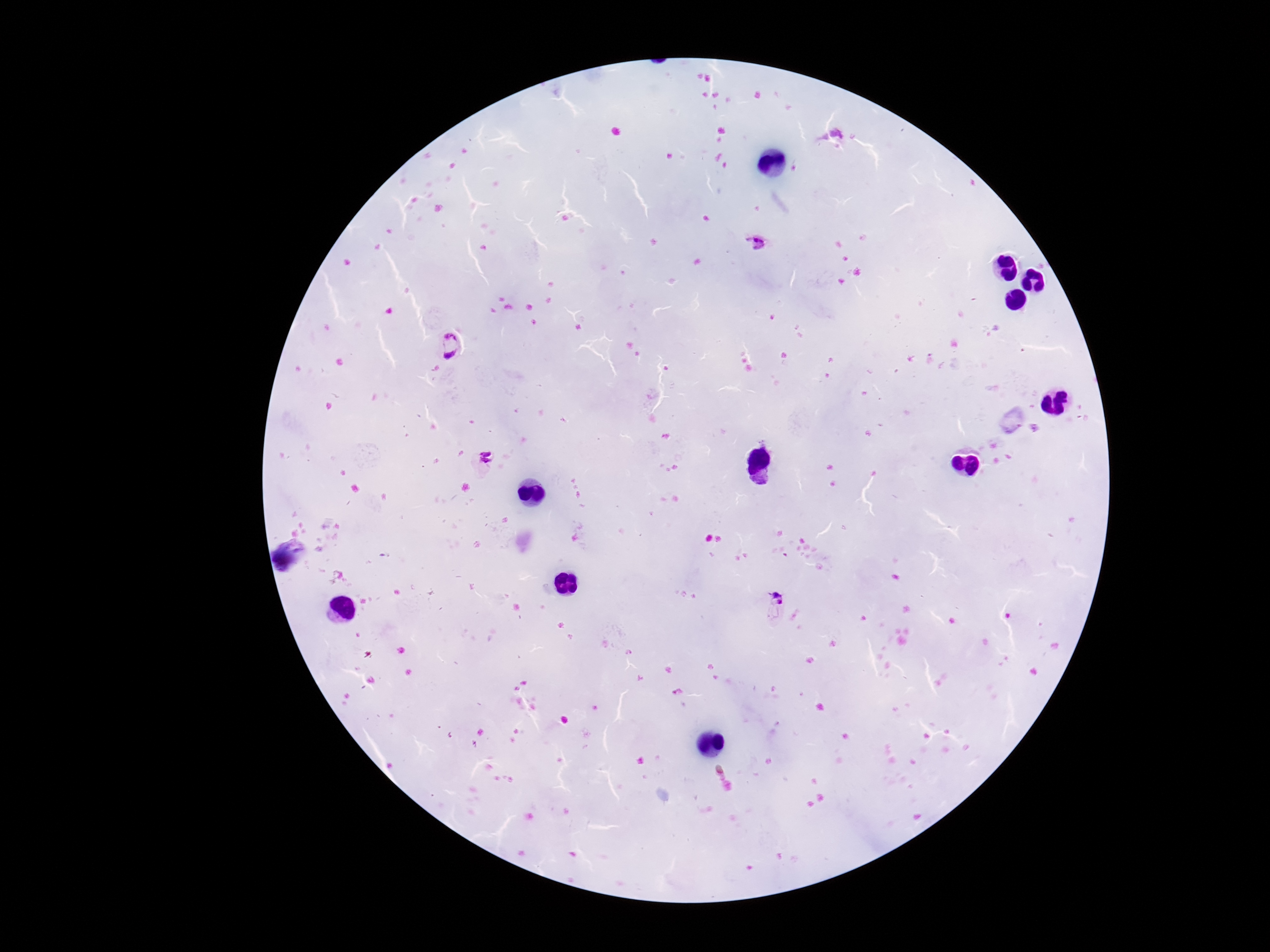

patient malaria status = positive
Plasmodium parasite locations = approximate centers as (x, y) in pixels: (759, 246), (451, 347), (480, 463), (777, 609)
field of view = single
stain = Giemsa
capture = smartphone camera through the microscope eyepiece
magnification = 100x
image size = 1270×952 pixels
preparation = thick peripheral-blood smear